Outline each blood parasite and name the species.
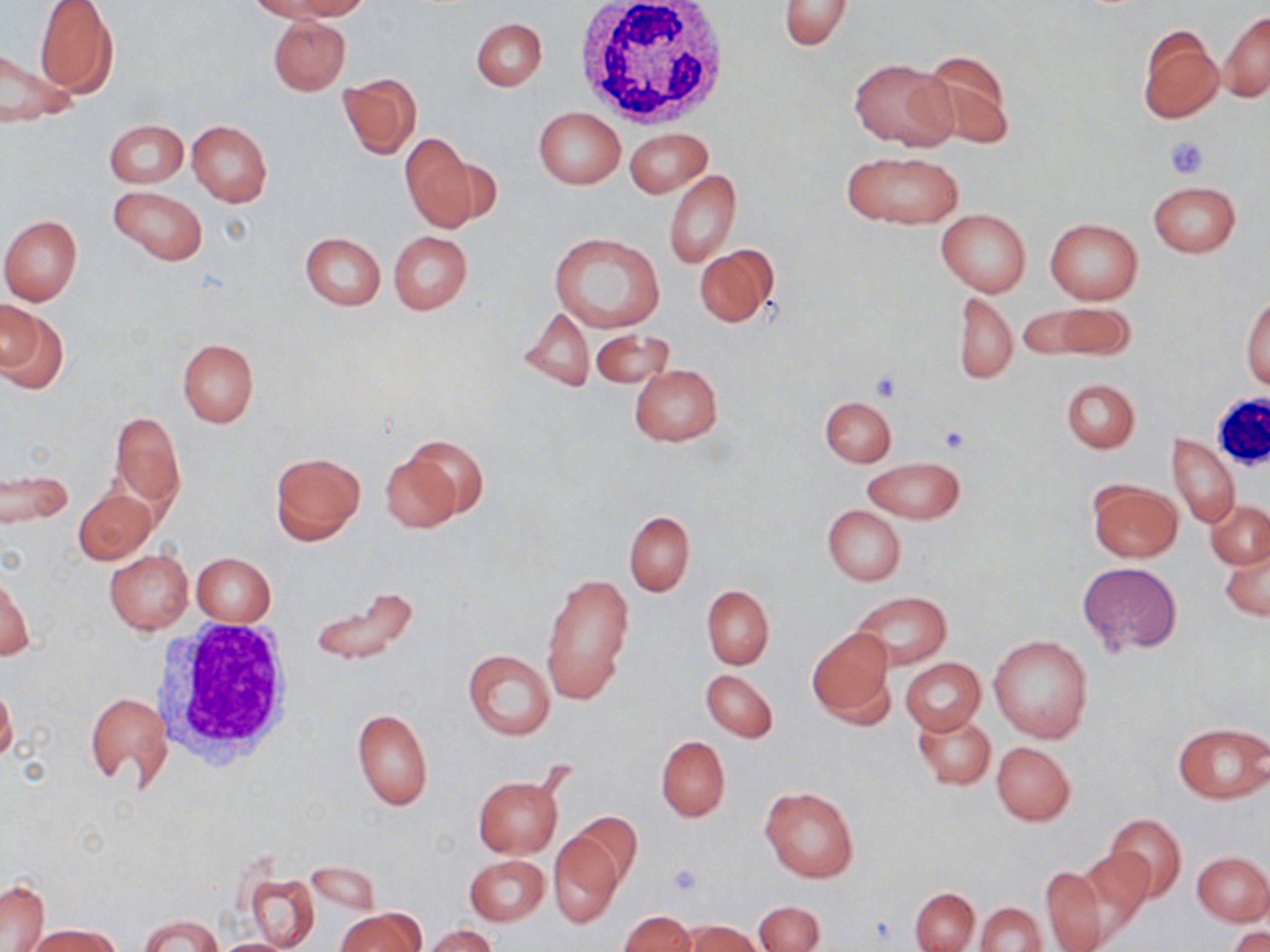
No blood parasites observed.

Approximate bounding boxes as [x1, y1, x2, y2] in pixels. Platelet locations: [1165, 135, 1209, 179], [867, 369, 906, 402], [938, 427, 971, 455], [667, 863, 703, 896]. White blood cell locations: [571, 0, 730, 127], [1211, 391, 1270, 471], [152, 623, 299, 772]. Uninfected red blood cell locations: [256, 0, 368, 22], [776, 1, 854, 51], [34, 2, 119, 98], [1219, 11, 1270, 101], [268, 15, 350, 95], [472, 17, 547, 90], [1136, 24, 1224, 124], [0, 46, 78, 130], [918, 48, 1015, 148], [851, 57, 956, 151], [338, 74, 421, 158], [534, 108, 624, 188], [187, 119, 272, 207], [104, 120, 187, 188], [625, 127, 711, 198], [399, 133, 481, 233], [841, 150, 964, 229], [664, 169, 740, 268], [1148, 180, 1241, 257], [107, 185, 208, 266], [936, 208, 1030, 296], [0, 215, 83, 304], [1045, 217, 1142, 304], [388, 231, 472, 314], [549, 232, 665, 333], [300, 233, 386, 310], [694, 244, 779, 328], [953, 292, 1017, 386], [1242, 297, 1270, 389], [1, 301, 69, 395], [1024, 302, 1135, 362], [518, 307, 594, 391], [590, 328, 674, 390], [177, 340, 258, 427], [629, 364, 723, 447], [1061, 378, 1140, 452], [820, 396, 896, 467], [109, 409, 186, 511], [1166, 433, 1240, 529], [404, 435, 490, 519], [380, 448, 466, 533], [269, 452, 365, 544], [863, 456, 965, 523], [0, 467, 72, 527], [1087, 479, 1181, 562], [75, 488, 156, 563], [1206, 500, 1270, 569], [822, 505, 906, 585], [623, 511, 694, 596], [1220, 541, 1269, 622], [104, 550, 193, 634], [191, 553, 276, 626], [1077, 562, 1182, 657], [542, 571, 634, 704], [1, 572, 33, 663], [310, 585, 417, 668], [701, 585, 774, 669], [851, 592, 951, 669], [807, 628, 895, 725], [989, 635, 1093, 742], [463, 649, 555, 740], [900, 657, 985, 734], [701, 668, 778, 742], [0, 683, 17, 763], [84, 690, 172, 791], [351, 707, 432, 810], [913, 712, 995, 789], [1173, 722, 1269, 802], [656, 735, 730, 822], [992, 742, 1075, 824], [472, 774, 564, 858], [760, 786, 859, 883], [568, 813, 643, 892], [1105, 814, 1187, 903], [547, 829, 622, 928], [1077, 846, 1153, 943], [1193, 852, 1270, 924], [465, 855, 549, 926], [307, 860, 382, 916], [1039, 865, 1108, 952], [245, 871, 320, 950], [1, 878, 49, 950], [910, 887, 980, 952], [753, 901, 823, 952], [977, 901, 1045, 952], [335, 909, 423, 952], [620, 910, 694, 952], [140, 915, 222, 951], [683, 921, 762, 952], [26, 923, 119, 952], [424, 925, 498, 952], [1228, 927, 1270, 952], [206, 938, 304, 951]. Slide-level diagnosis: no evidence of blood parasites. Optical microscopy. Captured at 1000x magnification. One field of a larger specimen. May-Grünwald-Giemsa-stained preparation. Image is 1270×952 pixels. Thin blood smear.